Comment on the morphology of the erythrocytes.
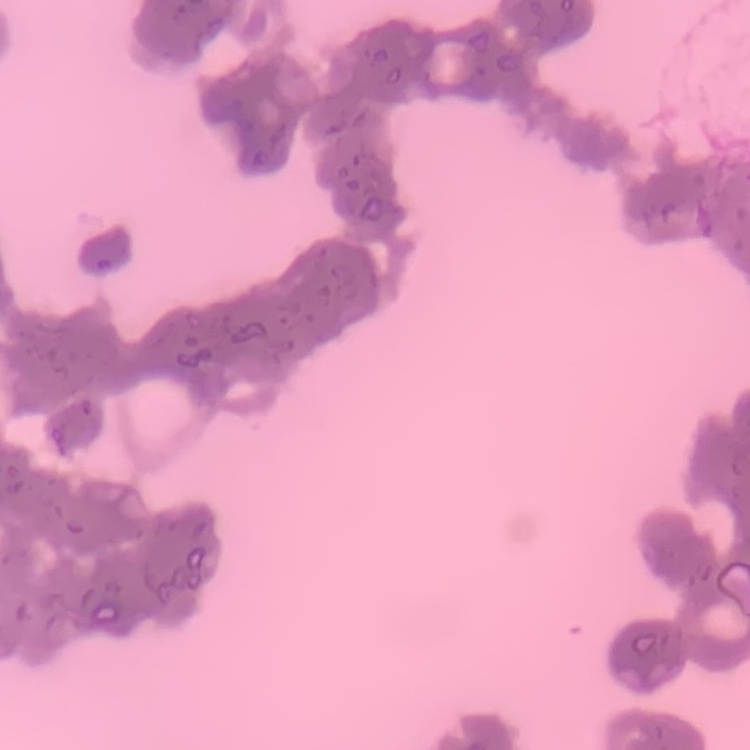

They show rouleaux formation.

Summary:
  - Image type: square crop of a larger photomicrograph
  - Preparation: thin peripheral smear
  - Stain: Field's or Giemsa